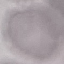

Result: no malaria parasites detected. Thin smear of blood. Acquired by smartphone through the microscope eyepiece. Giemsa-stained preparation. Automatically extracted cell patch, resized to 64 × 64 pixels.